Assess the morphology of the erythrocytes.
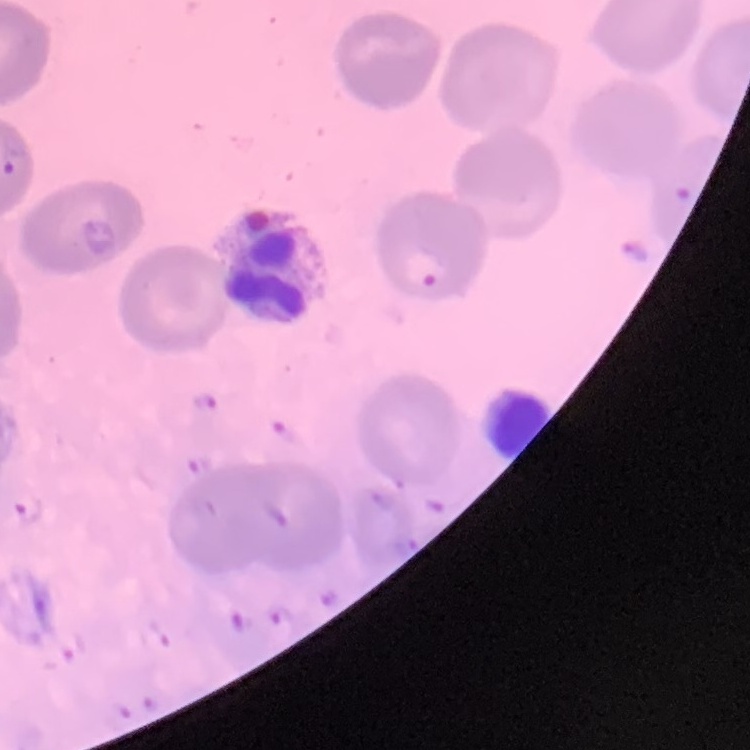
No rouleaux formation.

Field's or Giemsa stain. Thin peripheral smear. One tile cut from a larger photomicrograph.